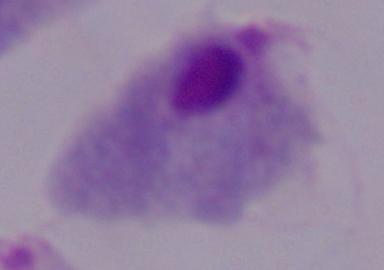 A trichomonad is seen. Micrograph. 1000x magnification.